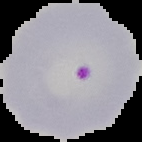
Summary:
  - Image size: 142×142 pixels
  - Image type: cell region segmented out of the field of view; surrounding area masked to black
  - Preparation: thin blood smear
  - Malaria status: parasitized